Identify the parasite.
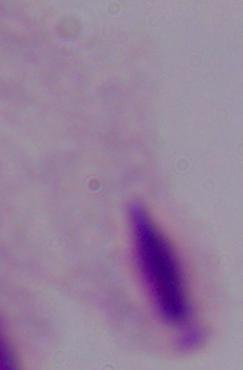

A trichomonad.

1000x magnification. Micrograph.